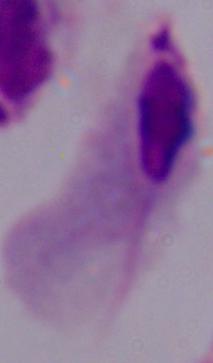

modality = photomicrograph
magnification = 1000x
identification = trichomonad